Assess this cell for malaria.
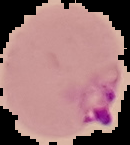

Parasitized.

Summary:
  - Preparation: thin blood smear
  - Image type: segmented cell region on a black background
  - Image size: 130×145 pixels